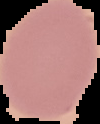
preparation = thin blood film
image size = 100×124 pixels
malaria status = uninfected
image type = segmented cell region with the area outside set to black